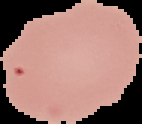

{
  "image_size": "142×124 pixels",
  "malaria_status": "uninfected",
  "image_type": "segmented cell region on a black background",
  "preparation": "thin blood film"
}